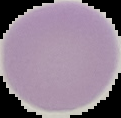
{
  "preparation": "thin blood smear",
  "image_type": "segmented cell region with the area outside set to black",
  "image_size": "121×118 pixels",
  "malaria_status": "uninfected"
}